State which parasite is depicted.
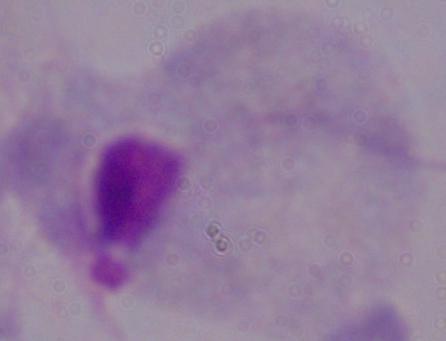

A trichomonad.

Summary:
  - Modality: photomicrograph
  - Magnification: 1000x